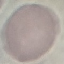

Summary:
  - Result: no malaria parasites detected
  - Preparation: thin blood film
  - Stain: Giemsa
  - Image type: automatically extracted cell patch, resized to 64 × 64 pixels
  - Capture: smartphone camera at the microscope eyepiece